Outline each uninfected red blood cell.
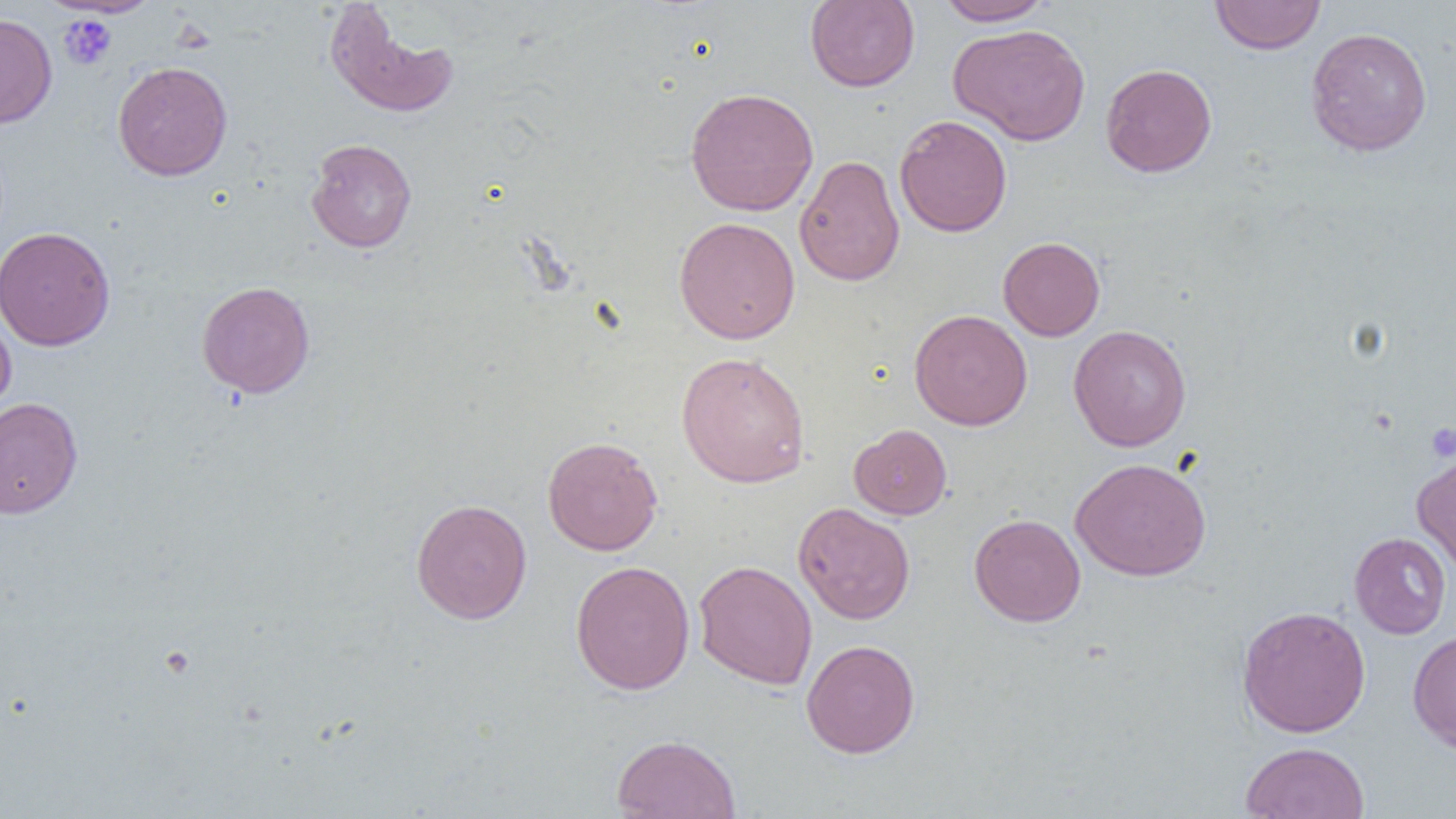

Approximate bounding boxes as (x1, y1, x2, y2) in pixels.
Uninfected red blood cells: (43, 0, 162, 18), (805, 0, 920, 92), (934, 0, 1056, 26), (1210, 0, 1326, 55), (324, 2, 459, 119), (0, 13, 57, 128), (949, 23, 1091, 145), (1305, 26, 1433, 157), (112, 60, 233, 180), (1100, 63, 1217, 177), (685, 87, 819, 217), (895, 114, 1012, 237), (306, 138, 417, 253), (794, 154, 904, 287), (674, 216, 800, 344), (0, 226, 115, 351), (997, 236, 1105, 341), (196, 281, 315, 398), (0, 307, 16, 415), (909, 309, 1033, 431), (1068, 324, 1192, 451), (676, 351, 811, 488), (0, 398, 83, 518), (849, 424, 952, 520), (542, 436, 663, 556), (1412, 450, 1456, 577), (1070, 457, 1211, 581), (411, 498, 532, 624), (793, 502, 915, 624), (969, 513, 1085, 627), (1349, 532, 1451, 639), (570, 560, 695, 695), (694, 560, 817, 690), (1236, 605, 1371, 737), (1407, 629, 1456, 753), (801, 639, 920, 758), (611, 733, 742, 819), (1240, 742, 1370, 819).

Summary:
  - Platelet locations: (59, 15, 117, 70), (1425, 422, 1456, 461)
  - Slide-level diagnosis: no evidence of blood parasites
  - Preparation: thin blood smear
  - Magnification: 1000x
  - Modality: light microscopy
  - Image size: 1456×819 pixels
  - Field of view: one of a larger specimen